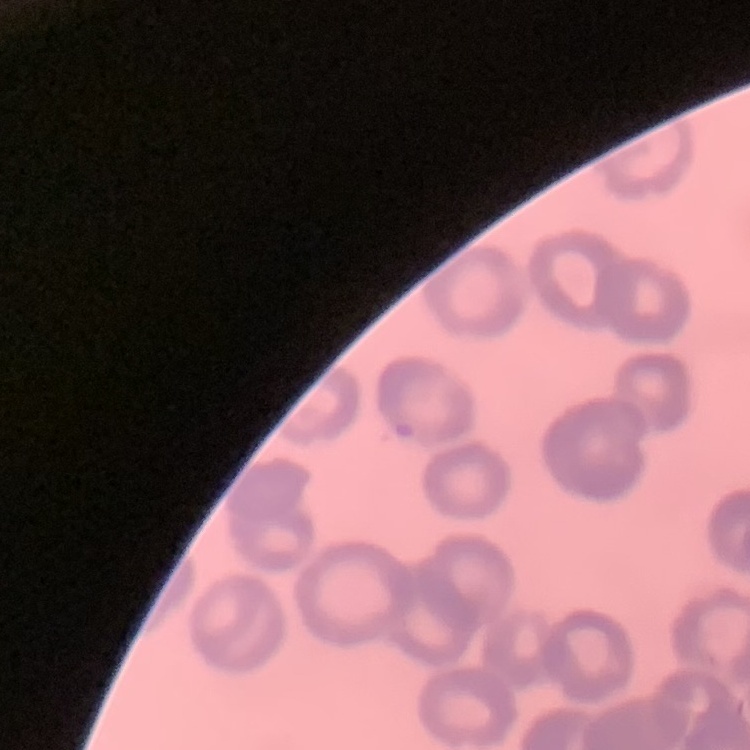 The red blood cells exhibit rouleaux formation. Thin peripheral smear. Square crop of a larger photomicrograph. Stained with either Field's or Giemsa.